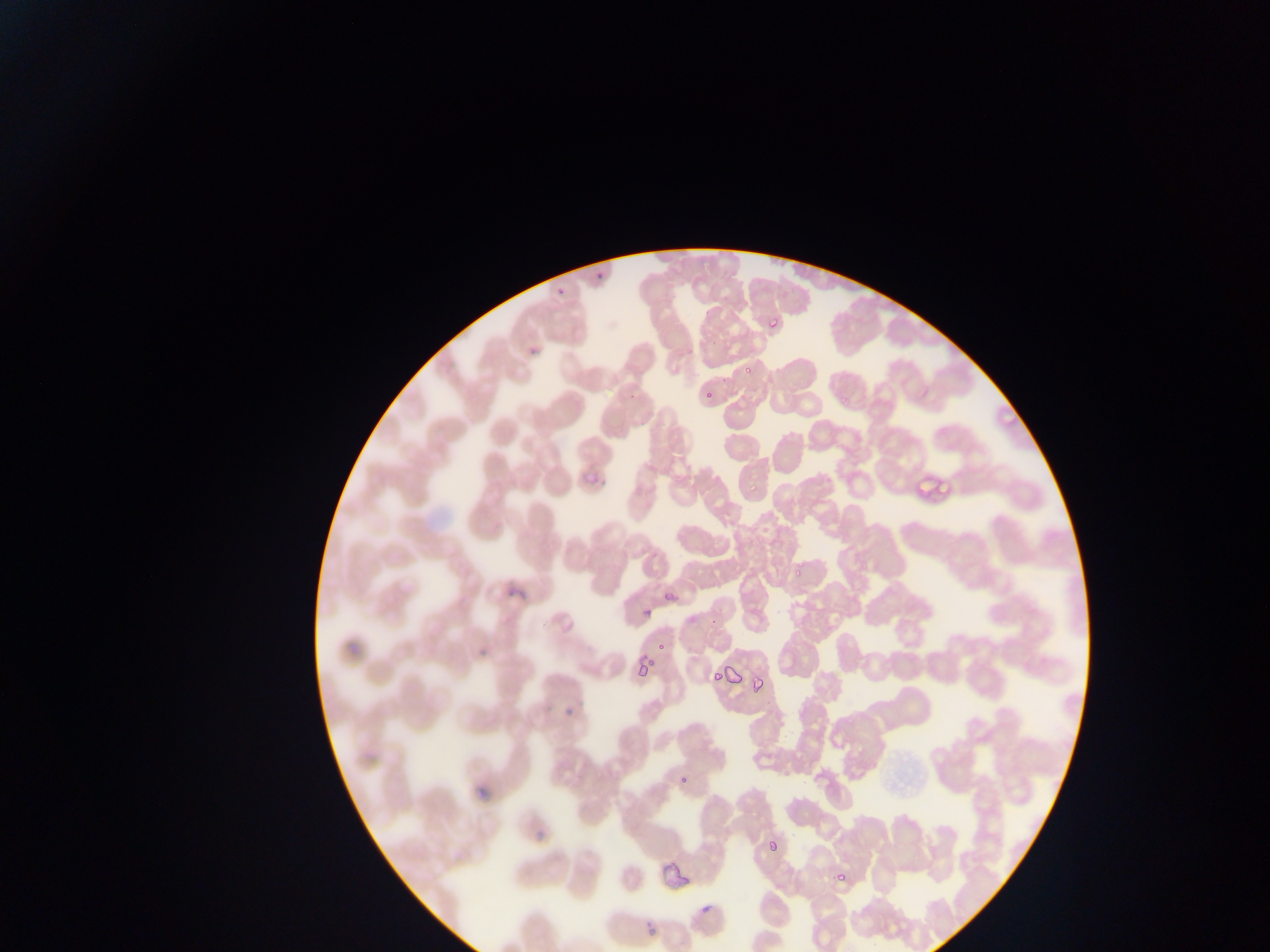 Approximate bounding boxes as (left, top, right, bottom) in pixels. Plasmodium parasite locations: (593, 274, 602, 283), (557, 281, 572, 298), (763, 315, 782, 332), (530, 341, 543, 358), (741, 369, 754, 375), (701, 385, 718, 399), (595, 478, 612, 493), (938, 482, 953, 499), (793, 568, 807, 579), (508, 578, 529, 595), (664, 586, 684, 604), (642, 604, 651, 619), (474, 635, 492, 667), (655, 638, 672, 656), (636, 663, 654, 674), (709, 669, 721, 683), (750, 676, 765, 694), (564, 698, 577, 718), (678, 775, 695, 788), (532, 813, 550, 844), (765, 829, 784, 854), (834, 875, 849, 891), (698, 900, 716, 913), (646, 928, 656, 936). Thin blood smear. Mobile-phone photograph taken through the microscope. One field of view. Sample from Ghana. Image is 1270×952 pixels.